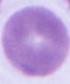
magnification: 1000x
modality: micrograph
identification: red blood cell